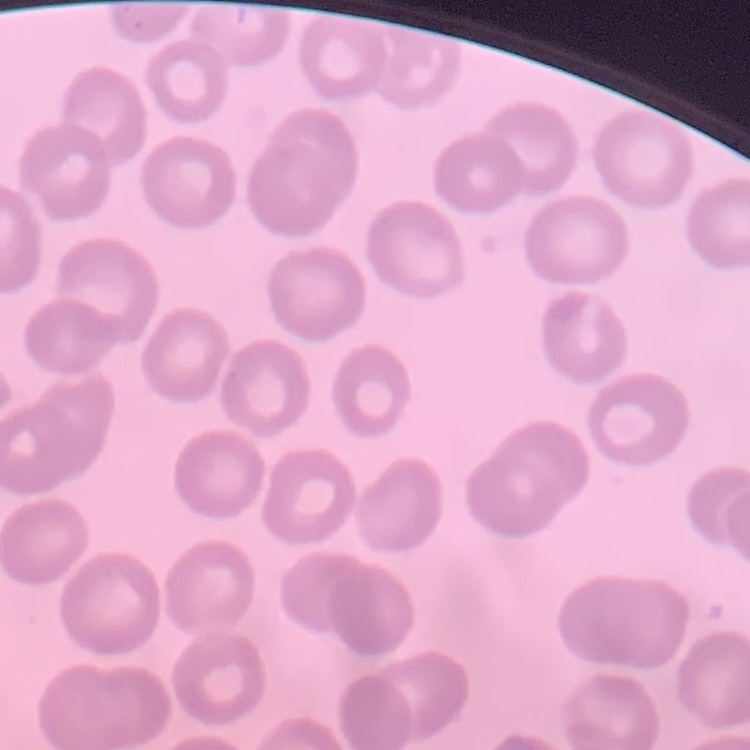 The red blood cells exhibit no rouleaux formation. Thin blood smear. Square crop of a larger photomicrograph. Stained with either Field's or Giemsa.